Assess the morphology of the erythrocytes.
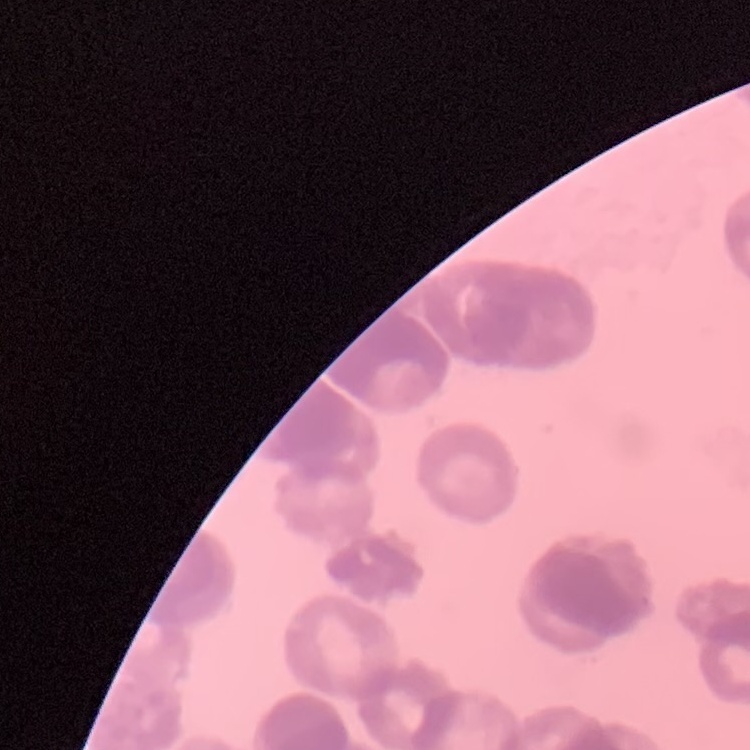
Rouleaux formation.

Square crop of a larger photomicrograph. Thin blood smear. Stained with either Field's or Giemsa.